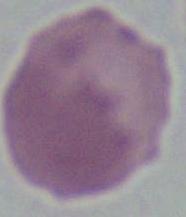 1000x magnification. Photomicrograph. A red blood cell is shown.